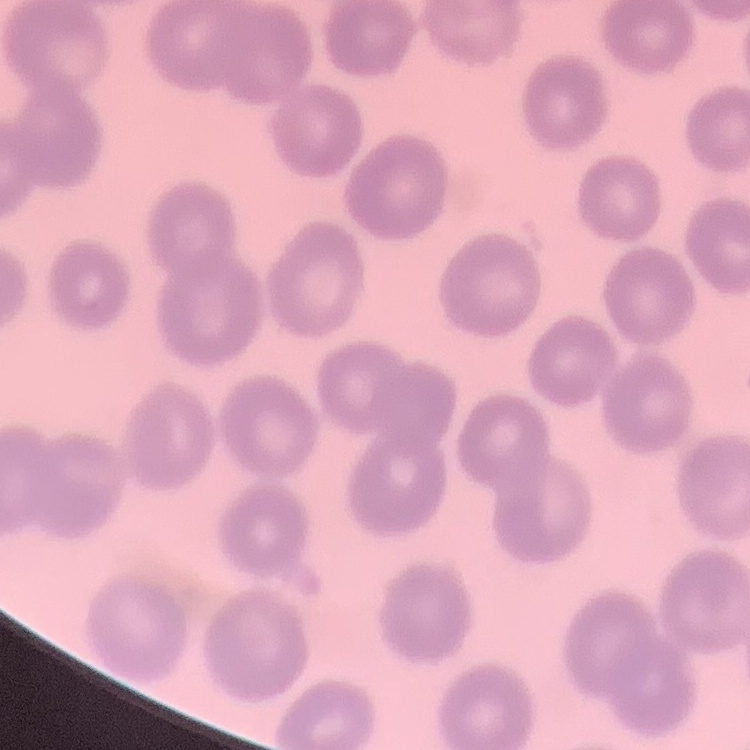
Summary:
  - Red blood cell morphology: no rouleaux formation
  - Stain: Field's or Giemsa
  - Preparation: thin blood smear
  - Image type: one tile cut from a larger photomicrograph